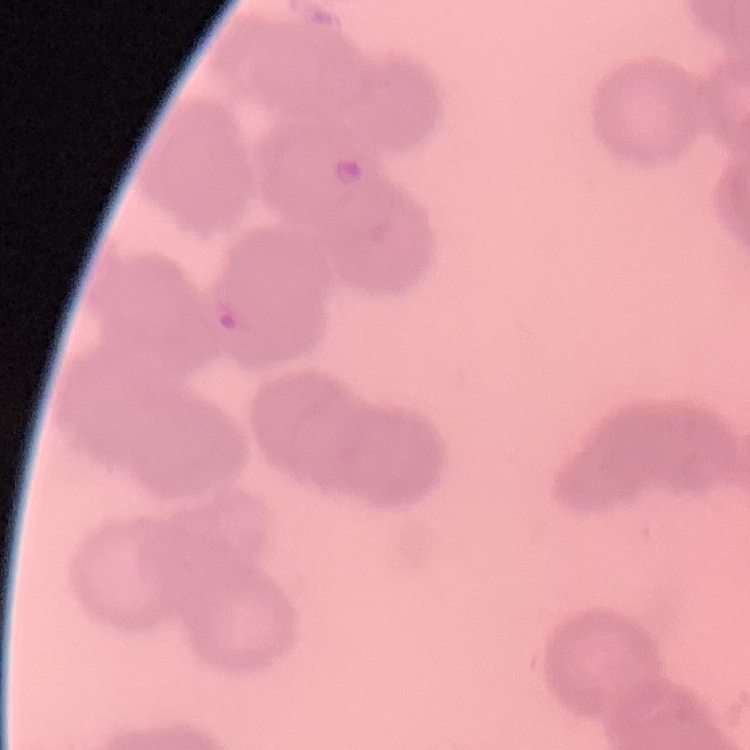
The erythrocytes show rouleaux formation. Field's or Giemsa stain. Thin blood film. Square crop of a larger photomicrograph.